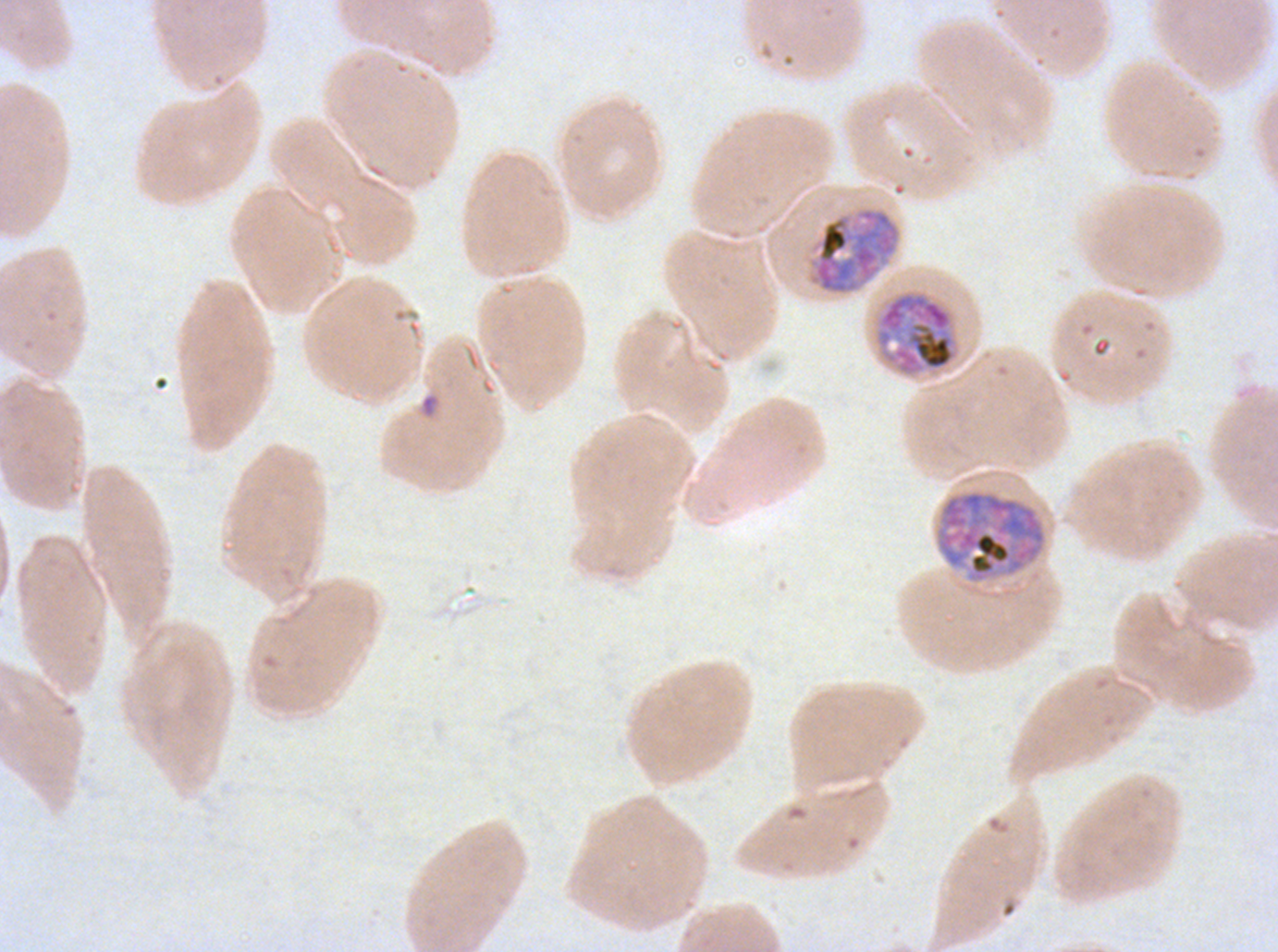
notation = approximate bounding boxes as (x1, y1, x2, y2) in pixels
late schizont locations = (874, 289, 960, 378), (935, 489, 1047, 583)
early schizont locations = (808, 206, 901, 295)
ring locations = (419, 392, 440, 419)
field of view = one sub-image of a larger composite
image size = 1278×952 pixels
stain = Giemsa
life-cycle stages observed = ring, early schizont, late schizont
preparation = thin blood smear
specimen = P. falciparum cultured ex vivo for 24 to 48 hours, from a patient in The Gambia